Locate and identify every blood parasite.
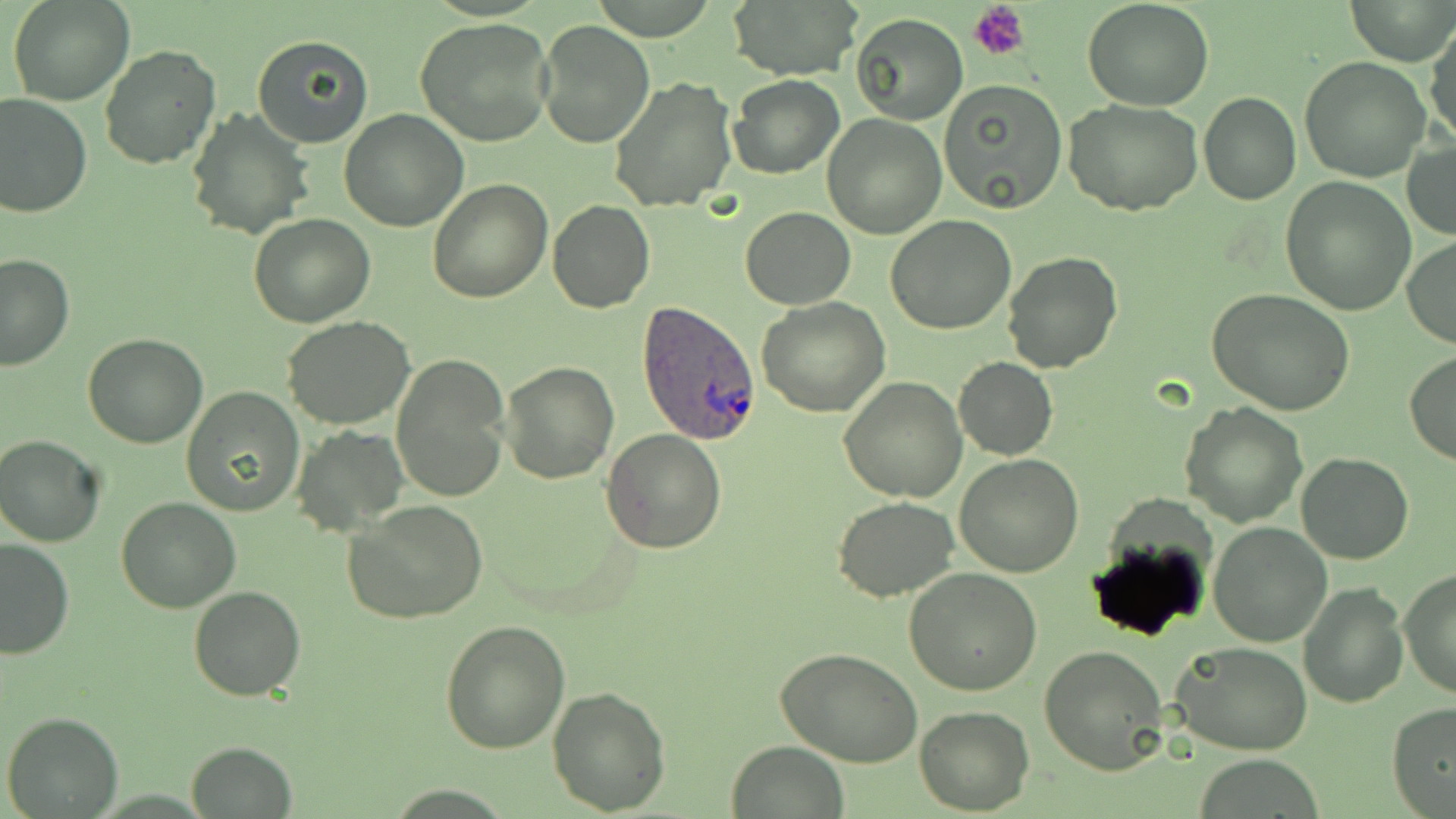

Approximate bounding boxes as named x1/y1/x2/y2 corners in pixels.
Plasmodium ovale-infected red blood cells: (x1=637, y1=300, x2=764, y2=444).
No Plasmodium falciparum, Plasmodium malariae, Plasmodium vivax, Babesia divergens, or Trypanosoma brucei observed.

slide-level diagnosis = Plasmodium ovale
platelet locations = approximate bounding boxes as named x1/y1/x2/y2 corners in pixels: (x1=970, y1=2, x2=1029, y2=61)
field of view = single
modality = light microscopy
stain = May-Grünwald-Giemsa
image size = 1456×819 pixels
uninfected red blood cell locations = approximate bounding boxes as named x1/y1/x2/y2 corners in pixels: (x1=8, y1=0, x2=132, y2=105), (x1=725, y1=0, x2=862, y2=82), (x1=1083, y1=0, x2=1214, y2=111), (x1=1346, y1=0, x2=1455, y2=66), (x1=849, y1=12, x2=967, y2=125), (x1=415, y1=18, x2=555, y2=147), (x1=536, y1=20, x2=654, y2=148), (x1=1427, y1=23, x2=1456, y2=148), (x1=252, y1=33, x2=376, y2=149), (x1=100, y1=44, x2=220, y2=171), (x1=1299, y1=56, x2=1431, y2=182), (x1=727, y1=74, x2=846, y2=180), (x1=610, y1=76, x2=738, y2=211), (x1=940, y1=80, x2=1069, y2=213), (x1=1199, y1=91, x2=1300, y2=205), (x1=0, y1=93, x2=92, y2=218), (x1=1064, y1=98, x2=1204, y2=216), (x1=186, y1=108, x2=313, y2=242), (x1=339, y1=109, x2=468, y2=231), (x1=822, y1=114, x2=947, y2=238), (x1=1403, y1=140, x2=1456, y2=240), (x1=1280, y1=177, x2=1416, y2=315), (x1=427, y1=178, x2=552, y2=301), (x1=547, y1=201, x2=656, y2=314), (x1=738, y1=206, x2=855, y2=309), (x1=249, y1=213, x2=376, y2=329), (x1=885, y1=216, x2=1017, y2=334), (x1=1403, y1=235, x2=1456, y2=348), (x1=1002, y1=251, x2=1124, y2=373), (x1=0, y1=253, x2=74, y2=372), (x1=1205, y1=288, x2=1354, y2=415), (x1=756, y1=297, x2=890, y2=418), (x1=280, y1=316, x2=416, y2=430), (x1=82, y1=332, x2=207, y2=449), (x1=1404, y1=351, x2=1456, y2=466), (x1=391, y1=353, x2=511, y2=503), (x1=954, y1=357, x2=1057, y2=461), (x1=500, y1=360, x2=619, y2=483), (x1=837, y1=376, x2=968, y2=501), (x1=182, y1=386, x2=305, y2=517), (x1=1180, y1=402, x2=1307, y2=527), (x1=291, y1=425, x2=410, y2=534), (x1=601, y1=430, x2=727, y2=554), (x1=0, y1=434, x2=107, y2=547), (x1=1296, y1=452, x2=1413, y2=564), (x1=953, y1=454, x2=1084, y2=577), (x1=833, y1=495, x2=960, y2=602), (x1=114, y1=497, x2=241, y2=613), (x1=343, y1=500, x2=490, y2=625), (x1=1207, y1=522, x2=1331, y2=647), (x1=1, y1=537, x2=77, y2=659), (x1=902, y1=567, x2=1044, y2=697), (x1=1400, y1=570, x2=1456, y2=699), (x1=1298, y1=580, x2=1407, y2=706), (x1=188, y1=584, x2=306, y2=701), (x1=439, y1=618, x2=571, y2=755), (x1=1172, y1=641, x2=1315, y2=754), (x1=1039, y1=645, x2=1170, y2=774), (x1=778, y1=647, x2=922, y2=768), (x1=546, y1=685, x2=671, y2=814), (x1=1387, y1=703, x2=1456, y2=818), (x1=914, y1=707, x2=1035, y2=814), (x1=2, y1=710, x2=124, y2=819), (x1=187, y1=740, x2=297, y2=817), (x1=726, y1=740, x2=850, y2=819)
magnification = 1000x
preparation = thin blood film